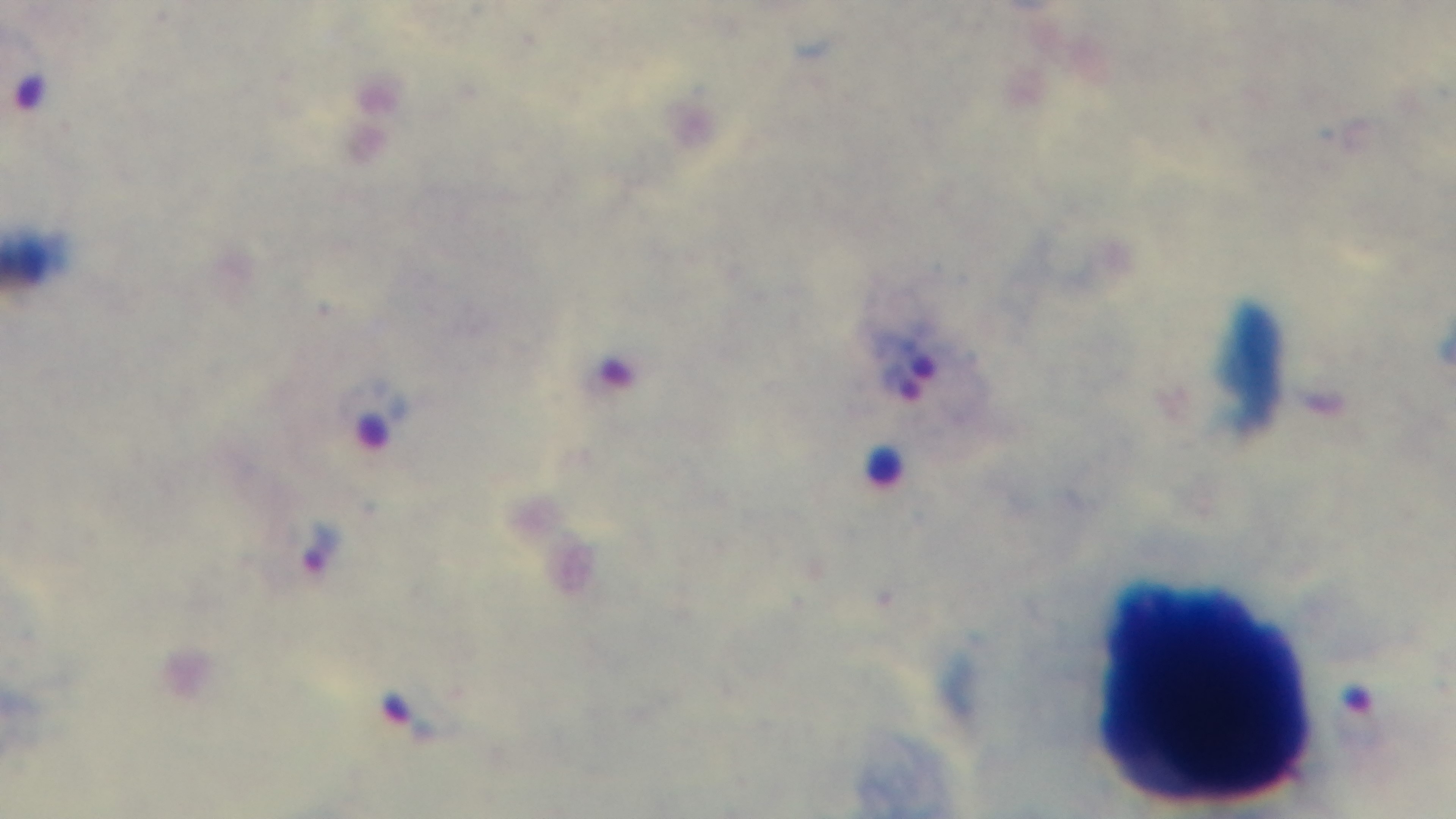

field of view = single
malaria status = positive
objective = 100x oil immersion
stain = Giemsa
preparation = thick blood film
capture = mounted 4K digital camera
modality = light microscopy